Name the parasite shown.
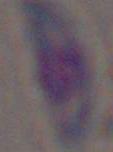
This is Toxoplasma gondii.

Micrograph. Captured at 1000x magnification.